Outline each P. falciparum parasite and classify it by life-cycle stage.
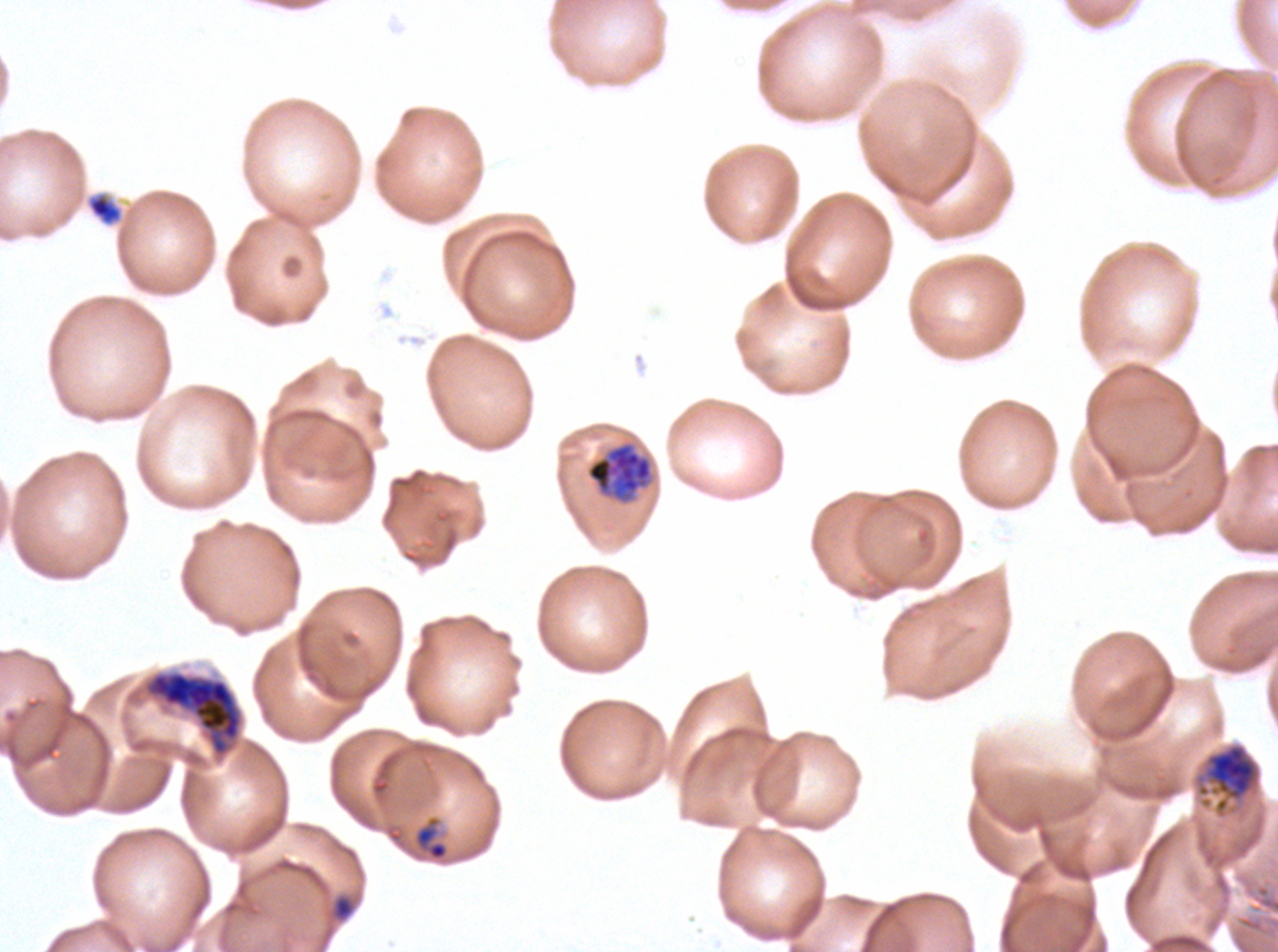

Approximate bounding rectangles given as corner coordinates in pixels from the top-left.
Late-ring/early-trophozoite forms: (x1=412, y1=815, x2=449, y2=861).
Early schizonts: (x1=586, y1=442, x2=653, y2=499), (x1=1194, y1=742, x2=1262, y2=816).
Late schizonts: (x1=144, y1=670, x2=243, y2=757).
No rings, mid trophozoites, late trophozoites, segmenters, or gametocytes observed.

Debris locations: (x1=88, y1=193, x2=122, y2=225), (x1=328, y1=892, x2=357, y2=923). Ex-vivo P. falciparum culture from a patient in The Gambia, grown for 24 to 48 hours. Giemsa-stained preparation. Life-cycle stages observed: late-ring/early-trophozoite, early schizont, late schizont. A sub-image separated from a larger composite. Image is 1278×952 pixels. Thin blood film.